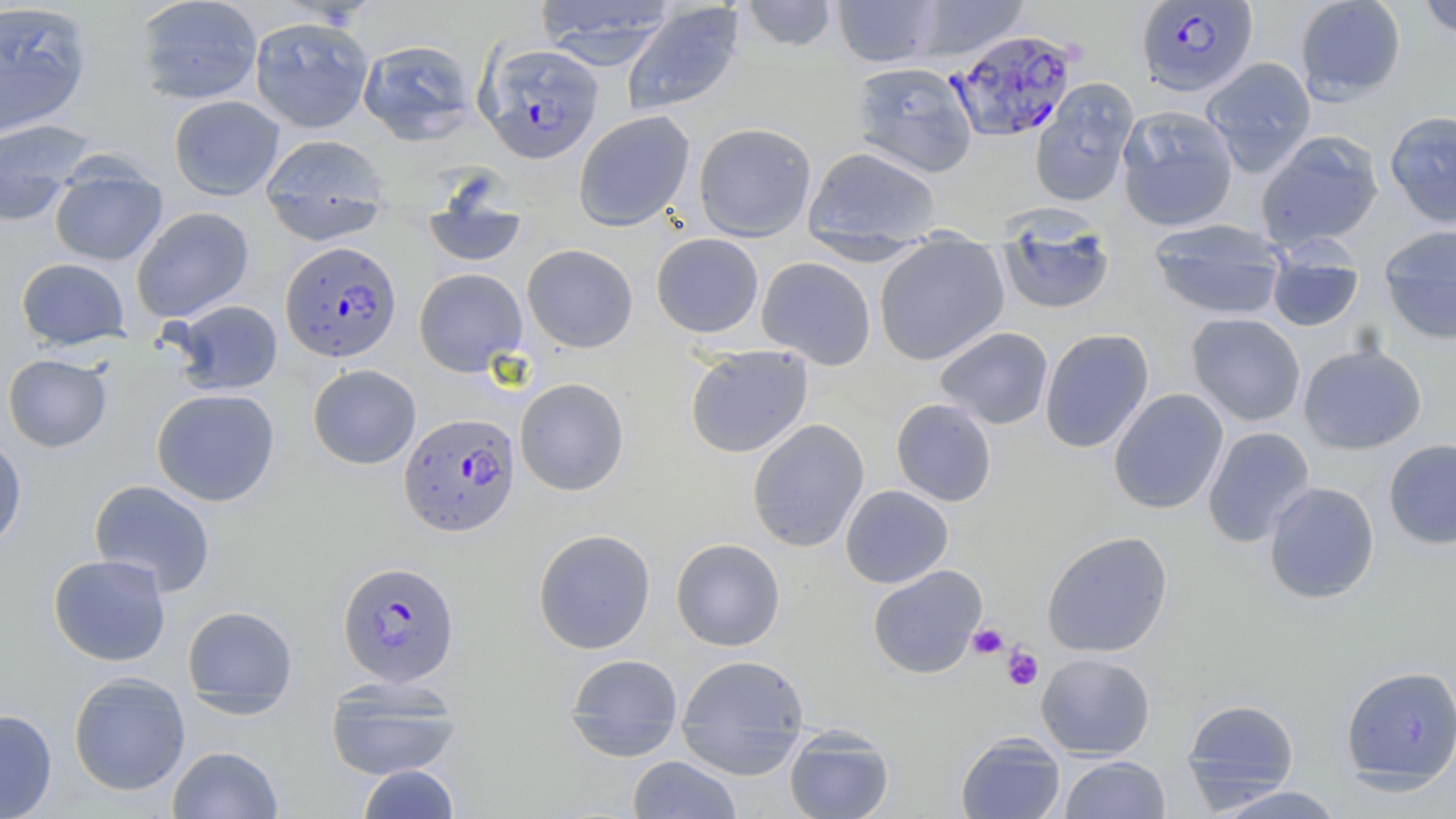
Approximate bounding boxes as named x1/y1/x2/y2 corners in pixels. Plasmodium falciparum-infected red blood cell locations: (x1=1135, y1=1, x2=1258, y2=97), (x1=948, y1=29, x2=1079, y2=143), (x1=479, y1=43, x2=604, y2=164), (x1=280, y1=241, x2=402, y2=363), (x1=398, y1=413, x2=521, y2=537), (x1=337, y1=560, x2=460, y2=687). Platelet locations: (x1=968, y1=623, x2=1008, y2=659), (x1=1003, y1=646, x2=1043, y2=690). Uninfected red blood cell locations: (x1=134, y1=0, x2=263, y2=105), (x1=534, y1=0, x2=677, y2=68), (x1=741, y1=0, x2=839, y2=52), (x1=833, y1=0, x2=943, y2=67), (x1=908, y1=0, x2=1029, y2=62), (x1=1295, y1=0, x2=1406, y2=102), (x1=1417, y1=0, x2=1456, y2=40), (x1=0, y1=2, x2=93, y2=137), (x1=621, y1=3, x2=746, y2=117), (x1=249, y1=15, x2=374, y2=133), (x1=357, y1=39, x2=478, y2=145), (x1=1202, y1=57, x2=1316, y2=176), (x1=851, y1=61, x2=977, y2=178), (x1=1030, y1=79, x2=1138, y2=207), (x1=169, y1=95, x2=285, y2=200), (x1=1117, y1=104, x2=1238, y2=232), (x1=1384, y1=109, x2=1456, y2=228), (x1=574, y1=110, x2=695, y2=231), (x1=0, y1=118, x2=95, y2=226), (x1=694, y1=122, x2=817, y2=242), (x1=1255, y1=130, x2=1384, y2=253), (x1=260, y1=134, x2=391, y2=244), (x1=803, y1=145, x2=942, y2=249), (x1=49, y1=163, x2=168, y2=267), (x1=423, y1=186, x2=528, y2=269), (x1=131, y1=206, x2=255, y2=323), (x1=996, y1=215, x2=1116, y2=316), (x1=1148, y1=218, x2=1288, y2=320), (x1=1379, y1=224, x2=1456, y2=345), (x1=651, y1=233, x2=764, y2=338), (x1=874, y1=242, x2=1009, y2=364), (x1=522, y1=243, x2=638, y2=352), (x1=1267, y1=243, x2=1364, y2=332), (x1=756, y1=256, x2=876, y2=369), (x1=16, y1=257, x2=130, y2=350), (x1=414, y1=268, x2=527, y2=376), (x1=170, y1=300, x2=283, y2=396), (x1=1186, y1=312, x2=1306, y2=426), (x1=934, y1=326, x2=1054, y2=430), (x1=1039, y1=328, x2=1155, y2=453), (x1=1298, y1=342, x2=1427, y2=455), (x1=685, y1=345, x2=813, y2=458), (x1=3, y1=353, x2=112, y2=453), (x1=308, y1=364, x2=421, y2=469), (x1=515, y1=377, x2=630, y2=496), (x1=151, y1=388, x2=280, y2=506), (x1=1108, y1=388, x2=1229, y2=514), (x1=891, y1=398, x2=997, y2=507), (x1=747, y1=418, x2=869, y2=553), (x1=1202, y1=426, x2=1316, y2=548), (x1=0, y1=435, x2=27, y2=553), (x1=1383, y1=438, x2=1456, y2=550), (x1=89, y1=479, x2=216, y2=597), (x1=1263, y1=482, x2=1380, y2=605), (x1=840, y1=485, x2=954, y2=589), (x1=532, y1=528, x2=656, y2=654), (x1=1041, y1=531, x2=1173, y2=657), (x1=670, y1=538, x2=786, y2=651), (x1=48, y1=554, x2=171, y2=666), (x1=867, y1=565, x2=987, y2=679), (x1=182, y1=605, x2=299, y2=715), (x1=564, y1=653, x2=684, y2=758), (x1=675, y1=653, x2=810, y2=773), (x1=1036, y1=653, x2=1156, y2=760), (x1=1340, y1=665, x2=1455, y2=790), (x1=68, y1=671, x2=191, y2=796), (x1=324, y1=676, x2=464, y2=781), (x1=1181, y1=698, x2=1300, y2=805), (x1=0, y1=708, x2=58, y2=818), (x1=784, y1=726, x2=894, y2=819), (x1=955, y1=732, x2=1066, y2=819), (x1=167, y1=745, x2=284, y2=818), (x1=1059, y1=755, x2=1171, y2=818), (x1=627, y1=756, x2=743, y2=818), (x1=357, y1=764, x2=461, y2=819), (x1=1209, y1=785, x2=1347, y2=818). Slide-level diagnosis: Plasmodium falciparum. Single field of view. Thin blood smear. Captured at 1000x magnification. Image is 1456×819 pixels. May-Grünwald-Giemsa stain. Light microscopy.